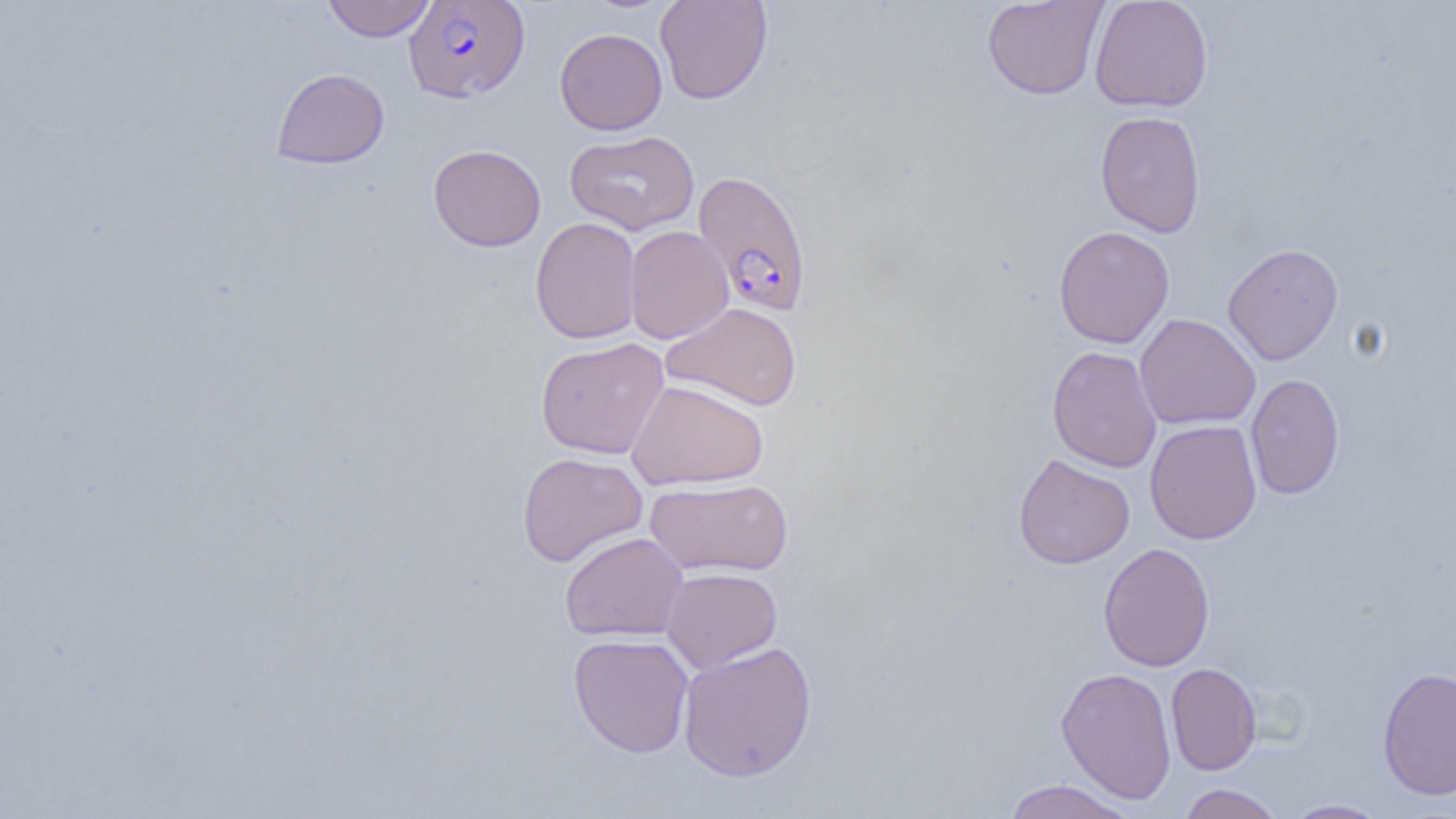
Approximate bounding boxes as named x1/y1/x2/y2 corners in pixels. Uninfected red blood cell locations: (x1=322, y1=0, x2=435, y2=42), (x1=655, y1=0, x2=773, y2=104), (x1=981, y1=0, x2=1109, y2=100), (x1=1089, y1=0, x2=1213, y2=113), (x1=554, y1=28, x2=667, y2=135), (x1=272, y1=68, x2=389, y2=169), (x1=1095, y1=111, x2=1206, y2=238), (x1=564, y1=130, x2=700, y2=236), (x1=428, y1=144, x2=546, y2=251), (x1=530, y1=217, x2=642, y2=344), (x1=624, y1=225, x2=733, y2=344), (x1=1053, y1=225, x2=1174, y2=348), (x1=1222, y1=242, x2=1343, y2=365), (x1=661, y1=302, x2=802, y2=411), (x1=1134, y1=313, x2=1261, y2=430), (x1=536, y1=337, x2=669, y2=459), (x1=1046, y1=345, x2=1162, y2=473), (x1=1245, y1=373, x2=1345, y2=500), (x1=626, y1=379, x2=769, y2=490), (x1=1144, y1=419, x2=1262, y2=544), (x1=517, y1=452, x2=648, y2=567), (x1=1013, y1=453, x2=1135, y2=569), (x1=644, y1=478, x2=794, y2=577), (x1=560, y1=531, x2=688, y2=642), (x1=1098, y1=542, x2=1215, y2=672), (x1=662, y1=567, x2=783, y2=672), (x1=568, y1=633, x2=695, y2=758), (x1=677, y1=640, x2=817, y2=782), (x1=1166, y1=663, x2=1262, y2=775), (x1=1377, y1=666, x2=1456, y2=800), (x1=1056, y1=667, x2=1177, y2=804), (x1=1002, y1=779, x2=1137, y2=819), (x1=1178, y1=783, x2=1284, y2=819), (x1=1282, y1=799, x2=1390, y2=818). Plasmodium falciparum-infected red blood cell locations: (x1=404, y1=0, x2=530, y2=103), (x1=693, y1=170, x2=812, y2=316). Slide-level diagnosis: Plasmodium falciparum. Light microscopy. Thin blood smear. Image is 1456×819 pixels. Single field of view. Captured at 1000x magnification.